Classify this cell by malaria status.
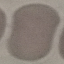

Uninfected.

Cell patch, automatically extracted from a larger field of view and resized to 64 × 64 pixels. Giemsa-stained preparation. Photographed with a smartphone camera at the microscope eyepiece. Thin smear of blood.